Report the malaria status of this cell.
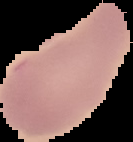
It is uninfected.

image size = 133×142 pixels
preparation = thin blood smear
image type = segmented cell region on a black background